Classify this cell by malaria status.
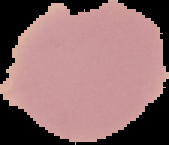

Uninfected.

Summary:
  - Image type: segmented cell region on a black background
  - Preparation: thin blood smear
  - Image size: 169×145 pixels